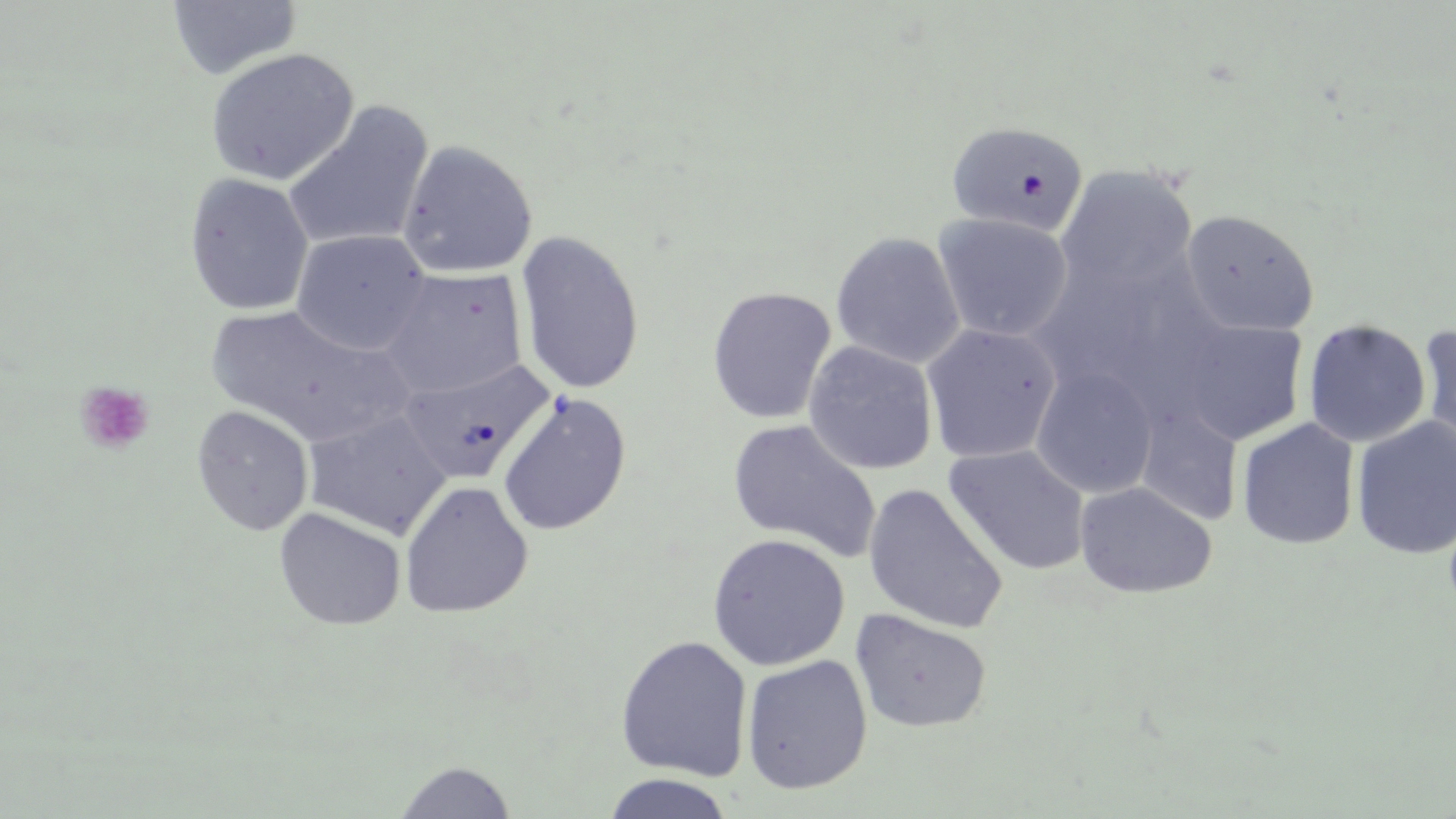

Approximate bounding boxes as (x1, y1, x2, y2) in pixels. Platelet locations: (75, 381, 154, 455). Uninfected red blood cell locations: (166, 1, 303, 81), (204, 48, 359, 186), (282, 101, 434, 253), (946, 120, 1089, 237), (397, 140, 538, 278), (1055, 164, 1198, 298), (184, 173, 313, 316), (1181, 209, 1320, 337), (933, 213, 1073, 342), (290, 228, 432, 356), (515, 230, 646, 395), (830, 231, 965, 369), (1040, 257, 1164, 392), (377, 267, 529, 399), (707, 286, 837, 425), (205, 304, 410, 451), (1303, 319, 1431, 448), (1175, 320, 1309, 445), (921, 322, 1062, 464), (1415, 325, 1456, 465), (803, 341, 939, 474), (399, 356, 555, 485), (1030, 365, 1159, 499), (495, 391, 633, 536), (1134, 402, 1243, 528), (190, 405, 314, 536), (303, 407, 452, 540), (1350, 416, 1456, 560), (728, 418, 882, 563), (1236, 418, 1360, 550), (943, 444, 1091, 576), (399, 480, 533, 618), (1075, 481, 1217, 598), (863, 483, 1008, 634), (274, 507, 406, 631), (707, 533, 851, 671), (850, 608, 992, 733), (615, 634, 753, 781), (741, 654, 873, 794), (394, 760, 517, 819), (600, 772, 735, 818). Slide-level diagnosis: negative for blood parasites. Optical microscopy. Thin blood smear. One field of a larger specimen. May-Grünwald-Giemsa stain. Image is 1456×819 pixels. Captured at 1000x magnification.